Give the position of every Plasmodium parasite visible.
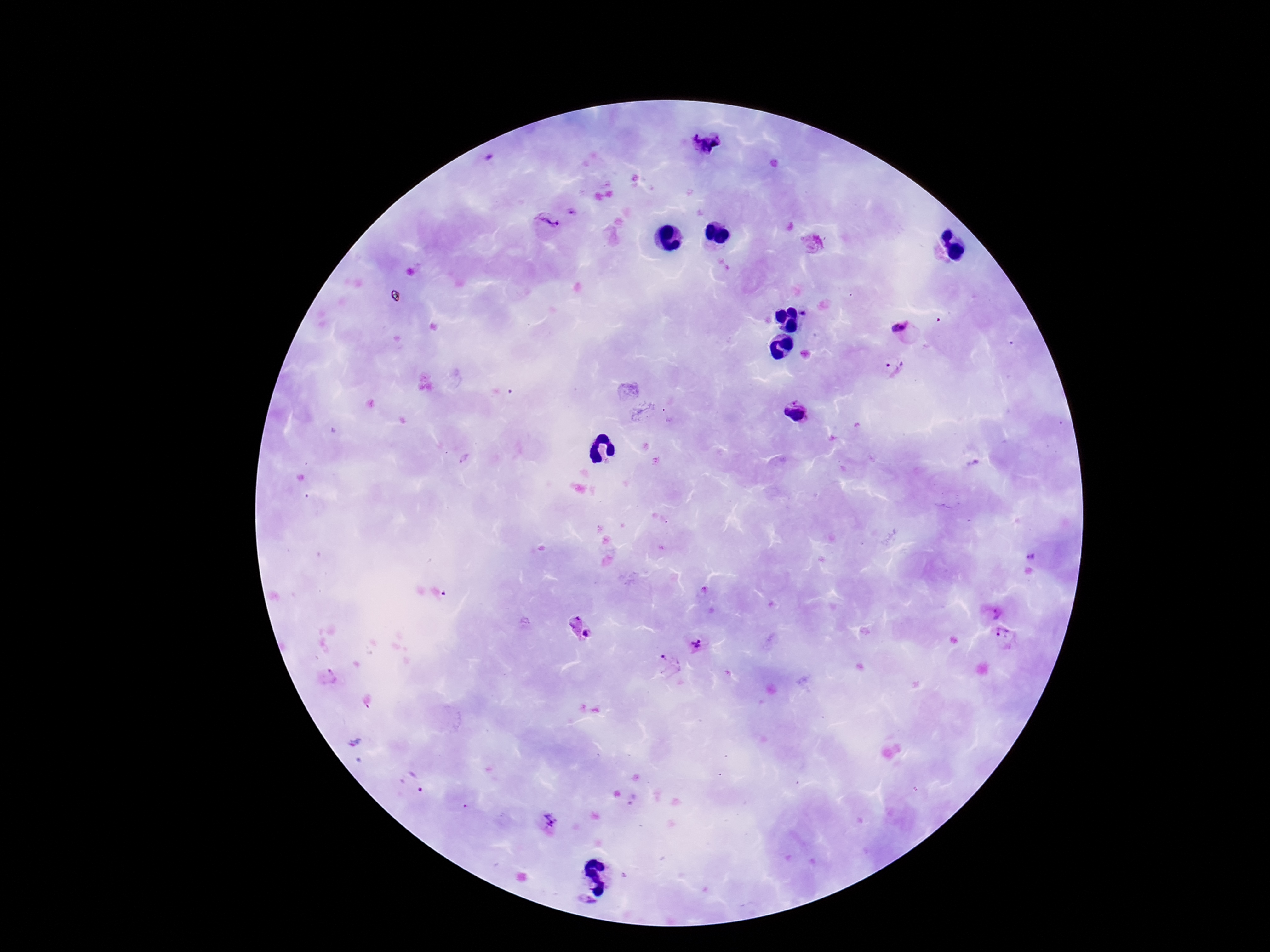

Approximate centers as [x, y] in pixels.
Plasmodium parasites: [707, 145], [574, 213], [548, 225], [812, 243], [805, 314], [903, 329], [893, 368], [795, 415], [655, 461], [1035, 555], [989, 613], [573, 626], [589, 634], [1005, 637], [696, 645], [668, 664], [413, 783], [547, 822], [586, 904].

patient malaria status = infected
stain = Giemsa
magnification = 100x
capture = smartphone camera through the microscope eyepiece
field of view = one from this slide
image size = 1270×952 pixels
preparation = thick peripheral-blood smear